Name the cell type shown.
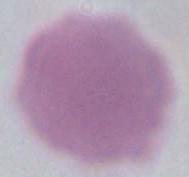

This is an erythrocyte.

modality: photomicrograph
magnification: 1000x